Give the position of every leukocyte visible.
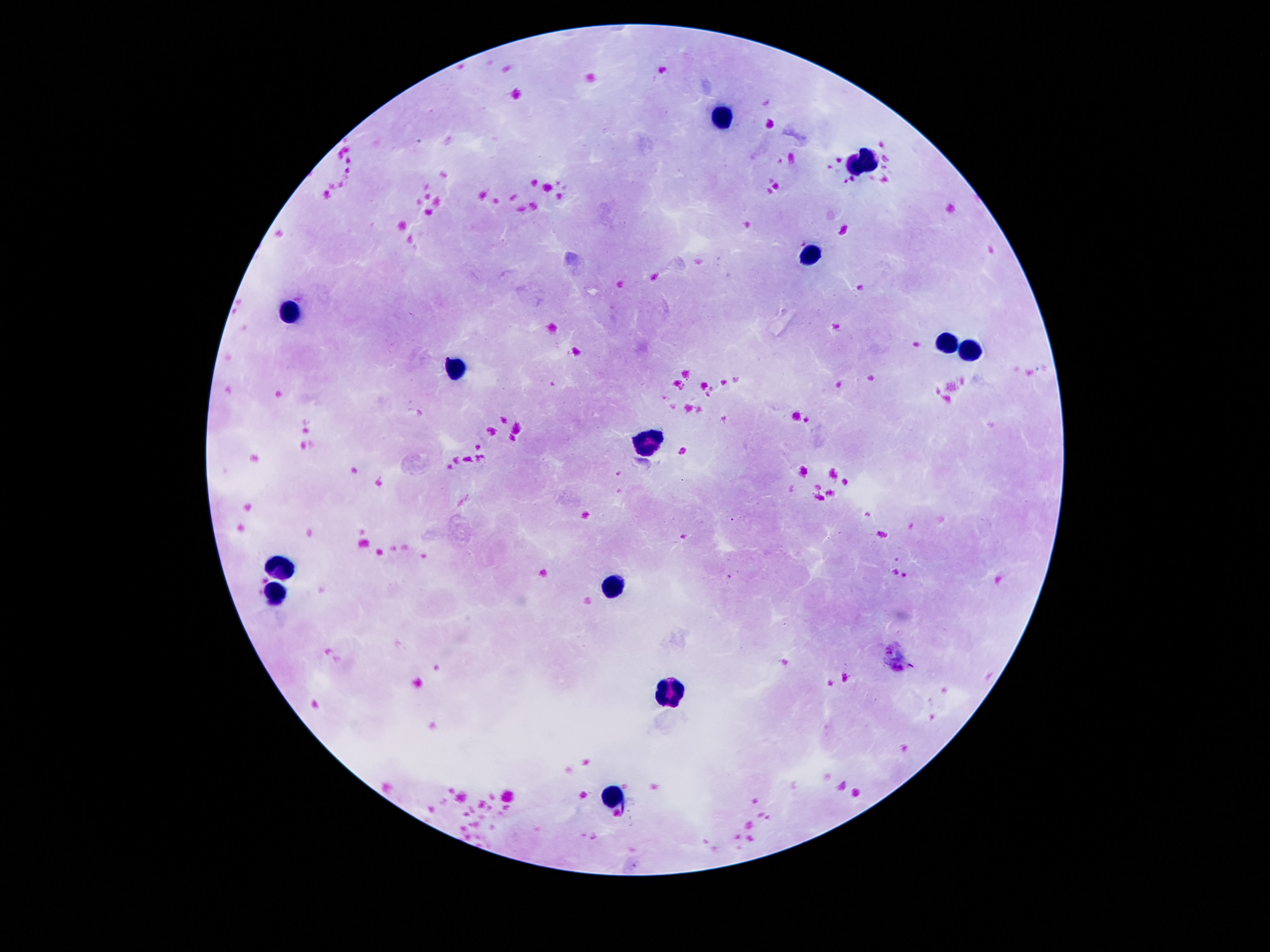
Approximate object centers, in pixels from the top-left corner.
Leukocytes: (x=723, y=121), (x=862, y=164), (x=810, y=253), (x=291, y=312), (x=946, y=343), (x=969, y=349), (x=457, y=370), (x=652, y=440), (x=281, y=568), (x=610, y=585), (x=279, y=590), (x=671, y=690), (x=616, y=793).

Thick peripheral-blood smear. Giemsa stain. 100x magnification. One field from this slide. Image is 1270×952 pixels. Patient malaria status: uninfected. Photographed through the microscope eyepiece with a smartphone camera.